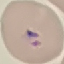
malaria status = parasitized
stain = Giemsa
capture = smartphone camera at the microscope eyepiece
preparation = thin smear
image type = cell patch, automatically extracted from a larger field of view and resized to 64 × 64 pixels